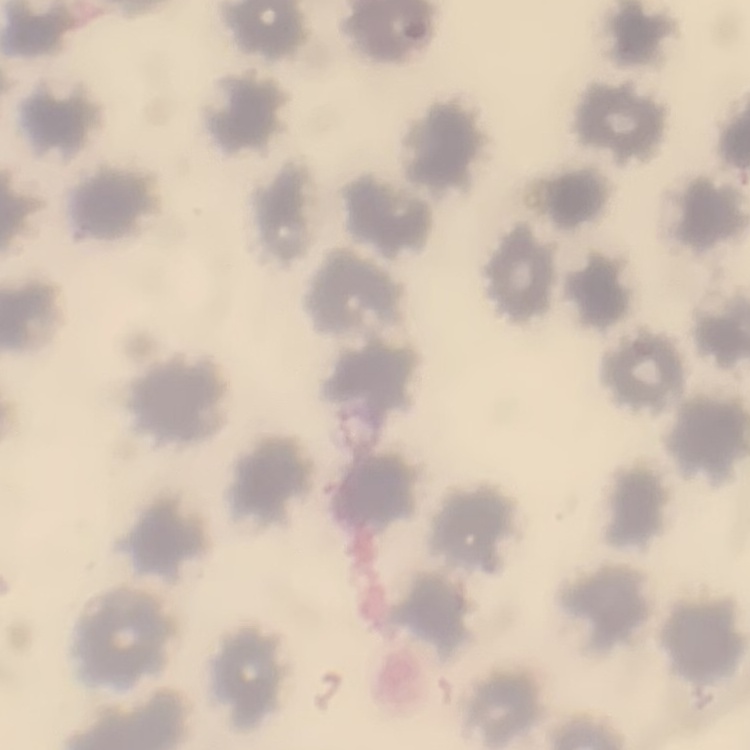

red blood cell morphology = no rouleaux formation
stain = Field's or Giemsa
preparation = thin blood smear
image type = square crop of a larger photomicrograph